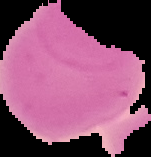
{
  "image_type": "segmented cell region on a black background",
  "preparation": "thin blood smear",
  "malaria_status": "uninfected",
  "image_size": "151×157 pixels"
}